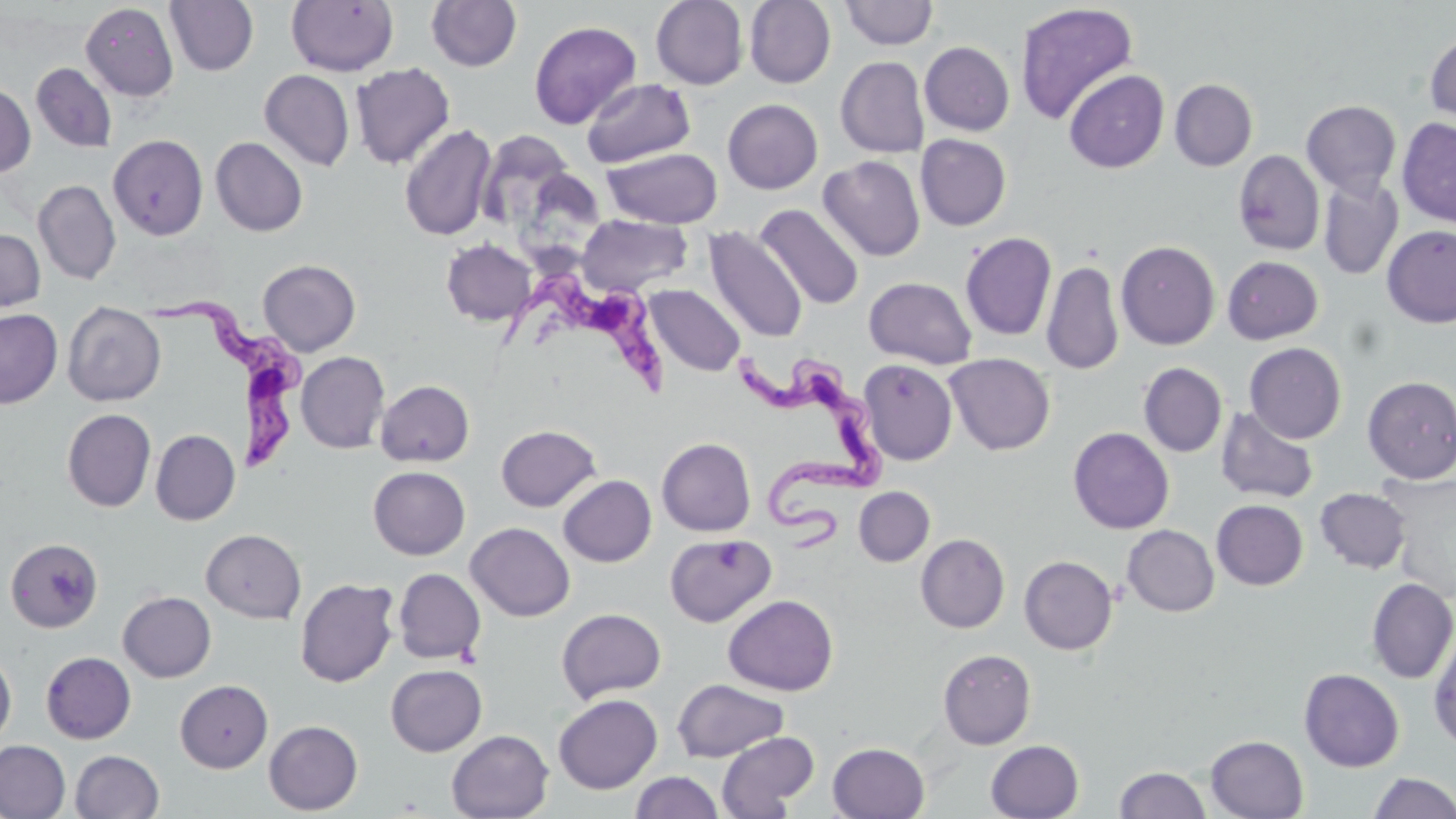
Summary:
  - Coordinate format: approximate bounding boxes as [x1, y1, x2, y2] in pixels
  - Uninfected red blood cell locations: [165, 0, 258, 75], [286, 0, 399, 76], [425, 0, 522, 72], [651, 0, 748, 89], [744, 0, 836, 88], [840, 1, 938, 49], [80, 2, 178, 102], [1015, 2, 1138, 126], [529, 20, 641, 129], [1425, 28, 1456, 132], [920, 41, 1014, 136], [836, 56, 929, 158], [31, 62, 117, 153], [350, 63, 455, 169], [259, 69, 355, 171], [1064, 69, 1168, 173], [581, 78, 695, 168], [1169, 79, 1257, 171], [0, 83, 35, 177], [723, 99, 823, 194], [1301, 100, 1401, 197], [1397, 118, 1456, 227], [399, 123, 497, 241], [480, 128, 574, 227], [108, 134, 209, 240], [915, 134, 1011, 230], [211, 137, 308, 237], [602, 147, 723, 229], [1233, 150, 1325, 256], [819, 155, 925, 261], [515, 172, 601, 275], [1318, 175, 1403, 280], [33, 180, 121, 285], [755, 204, 864, 310], [577, 213, 692, 296], [704, 226, 807, 342], [1382, 226, 1456, 328], [0, 229, 46, 312], [960, 231, 1056, 341], [441, 238, 537, 326], [1116, 241, 1220, 350], [1222, 255, 1323, 344], [258, 259, 361, 356], [1041, 259, 1124, 375], [863, 277, 978, 368], [644, 285, 746, 376], [62, 301, 166, 406], [0, 309, 62, 408], [1244, 342, 1346, 444], [296, 352, 390, 453], [944, 354, 1055, 456], [857, 360, 958, 465], [1138, 362, 1227, 457], [1362, 376, 1456, 483], [375, 380, 474, 467], [1216, 406, 1319, 504], [62, 409, 156, 512], [495, 424, 601, 511], [1068, 427, 1174, 534], [150, 429, 240, 525], [657, 437, 756, 536], [368, 466, 470, 560], [1376, 471, 1456, 601], [558, 475, 656, 567], [854, 487, 935, 567], [1315, 488, 1411, 573], [1212, 500, 1308, 590], [465, 522, 575, 622], [1122, 525, 1219, 617], [201, 529, 306, 623], [665, 533, 777, 627], [916, 534, 1010, 633], [5, 538, 103, 632], [1019, 555, 1118, 655], [393, 568, 486, 664], [295, 577, 399, 687], [1366, 578, 1456, 683], [118, 591, 216, 682], [723, 594, 838, 695], [556, 607, 667, 704], [1429, 626, 1456, 752], [0, 649, 16, 747], [937, 649, 1036, 749], [41, 651, 136, 744], [385, 664, 487, 756], [1299, 669, 1405, 772], [175, 679, 273, 772], [672, 679, 789, 762], [553, 694, 662, 794], [264, 720, 363, 814], [446, 730, 554, 818], [716, 731, 819, 818], [1205, 735, 1308, 818], [0, 739, 70, 819], [985, 740, 1084, 818], [828, 741, 929, 819], [70, 750, 165, 818], [1115, 766, 1211, 818], [630, 771, 725, 819], [1369, 772, 1456, 819]
  - Trypanosoma brucei locations: [496, 271, 669, 395], [143, 290, 310, 469], [733, 344, 886, 557]
  - Slide-level diagnosis: Trypanosoma brucei
  - Modality: optical microscopy
  - Image size: 1456×819 pixels
  - Stain: May-Grünwald-Giemsa
  - Preparation: thin blood film
  - Magnification: 1000x
  - Field of view: single